Give a bounding box for every parasitised red blood cell.
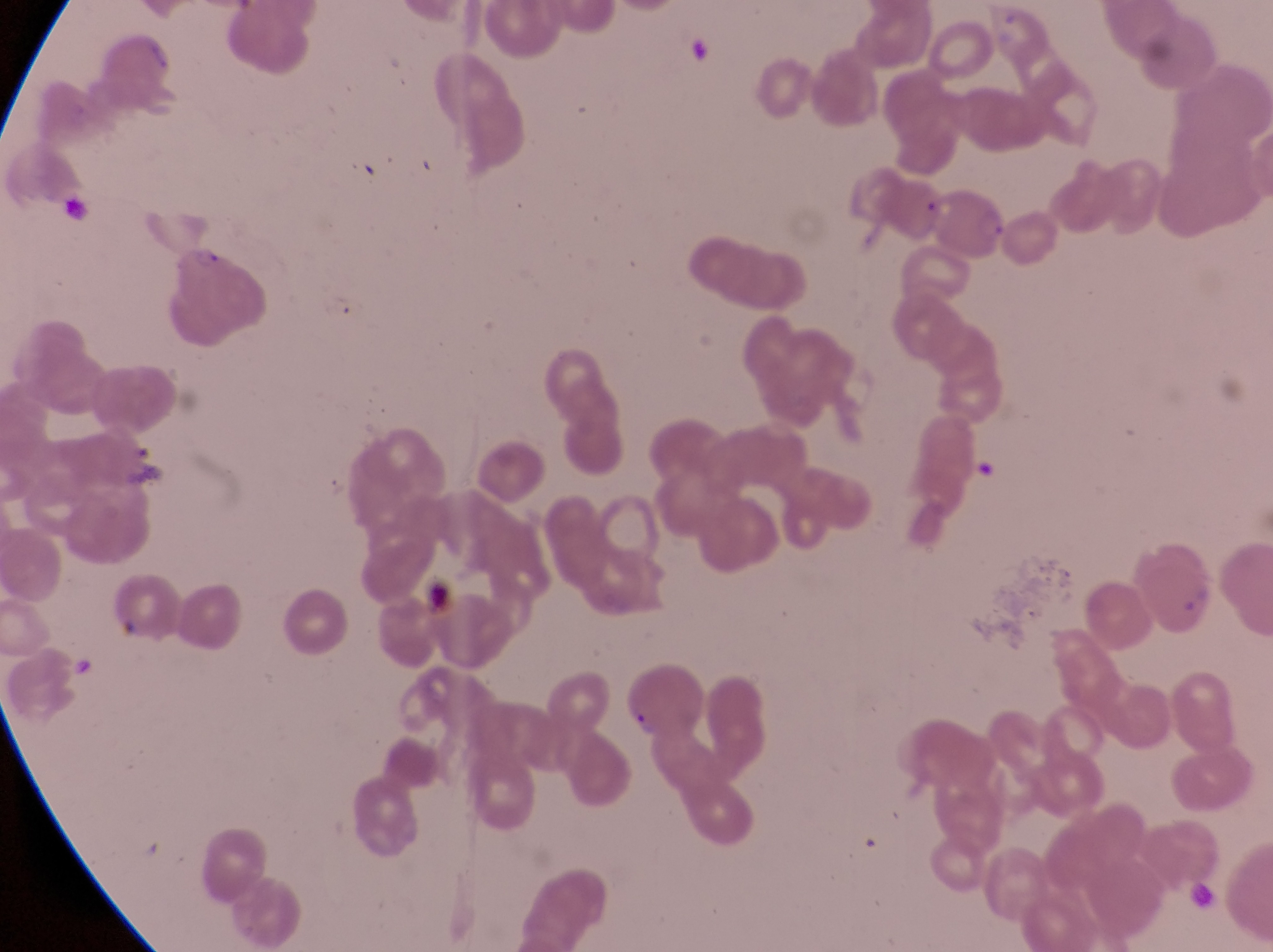

Approximate bounding boxes as left top right bottom in pixels.
Parasitised red blood cells: 931 183 1009 260; 172 242 269 349.

magnification = 1000x
artifact (platelet-like body, stain precipitate, or debris) locations = approximate bounding boxes as left top right bottom in pixels: 976 450 999 478; 412 564 455 619
image size = 1273×952 pixels
preparation = thin blood smear
country = Uganda
field of view = single
capture = smartphone photograph through the eyepiece of an Olympus CX-23 microscope